Describe the morphology of the erythrocytes.
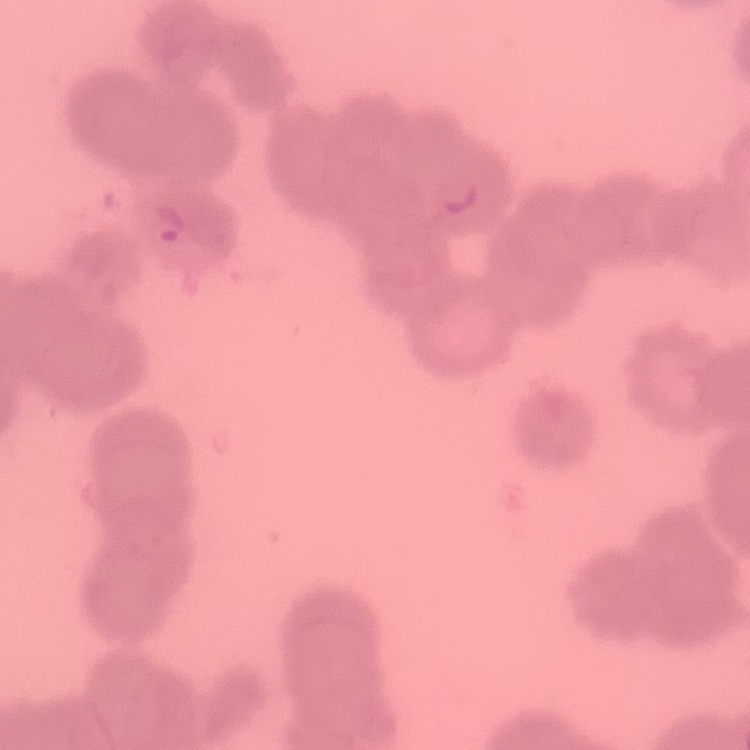
They show rouleaux formation.

Summary:
  - Preparation: thin peripheral smear
  - Image type: square crop of a larger photomicrograph
  - Stain: Field's or Giemsa